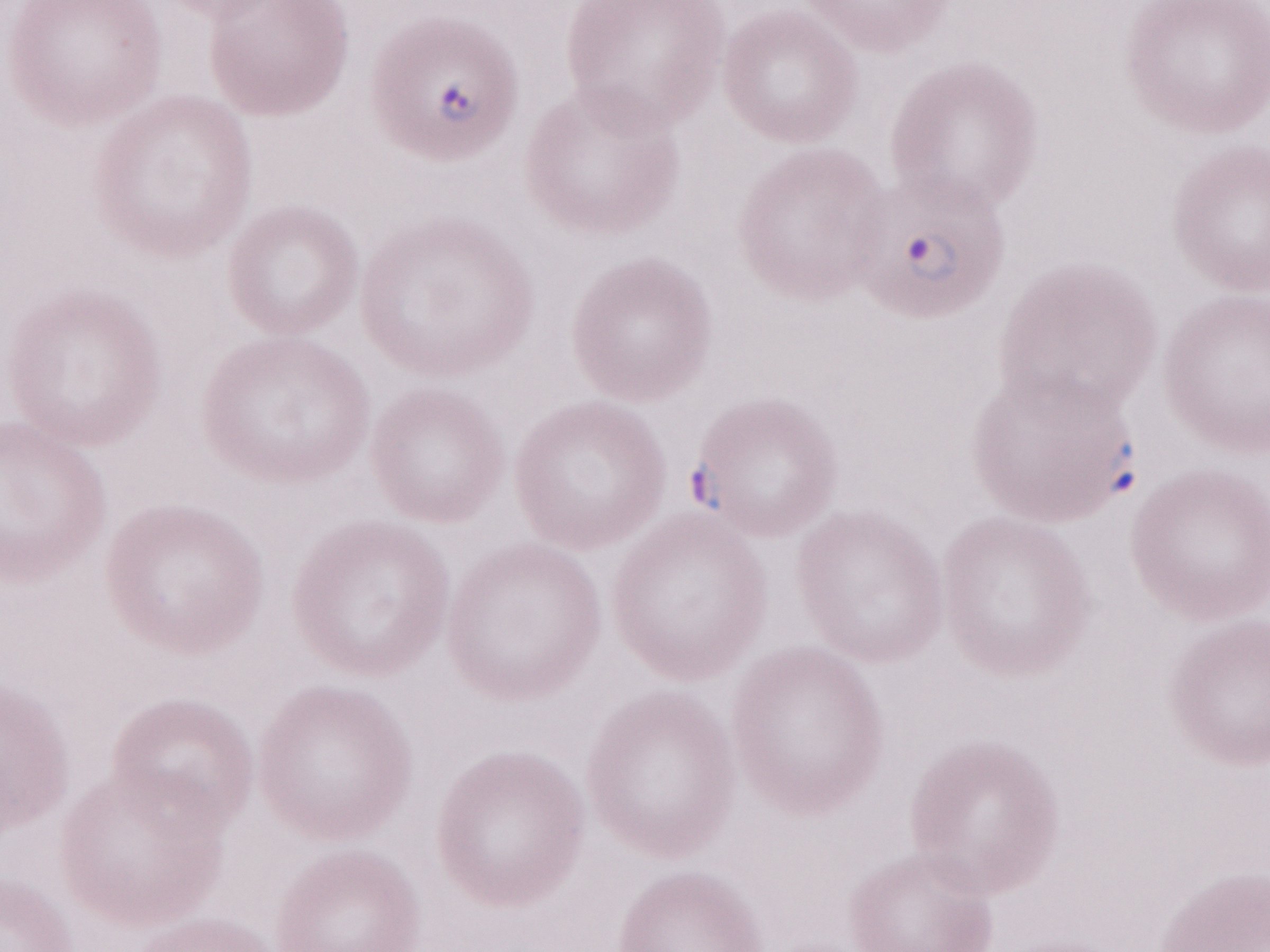
Malaria diagnosis (patient-level): positive. 1,000x magnification. One field of this slide. Thin blood film. Olympus BX43 microscope and DP73 digital camera. Image is 1270×952 pixels. May-Grünwald-Giemsa (MGG) stain.